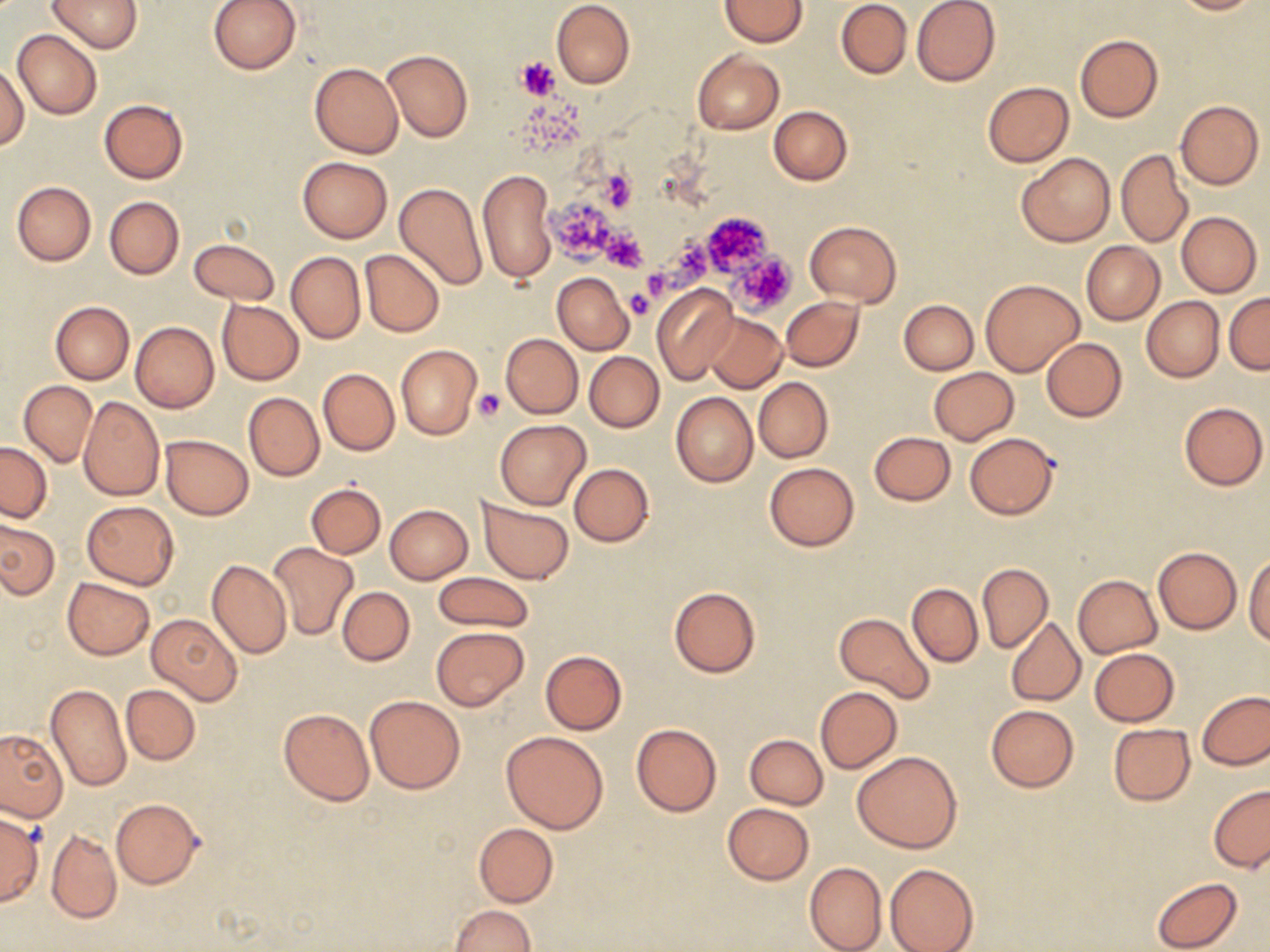
Summary:
  - Coordinate format: approximate bounding boxes as named x1/y1/x2/y2 corners in pixels
  - Platelet locations: (x1=514, y1=56, x2=560, y2=99), (x1=598, y1=166, x2=637, y2=213), (x1=549, y1=199, x2=618, y2=264), (x1=700, y1=212, x2=773, y2=276), (x1=601, y1=229, x2=647, y2=273), (x1=660, y1=234, x2=709, y2=286), (x1=732, y1=251, x2=797, y2=315), (x1=625, y1=290, x2=655, y2=319), (x1=474, y1=389, x2=504, y2=419)
  - Uninfected red blood cell locations: (x1=47, y1=0, x2=142, y2=53), (x1=209, y1=0, x2=300, y2=74), (x1=551, y1=0, x2=635, y2=88), (x1=720, y1=0, x2=808, y2=46), (x1=836, y1=0, x2=911, y2=79), (x1=912, y1=0, x2=1001, y2=86), (x1=1171, y1=0, x2=1259, y2=15), (x1=12, y1=29, x2=101, y2=120), (x1=1074, y1=34, x2=1163, y2=122), (x1=382, y1=49, x2=473, y2=141), (x1=692, y1=49, x2=784, y2=134), (x1=309, y1=62, x2=402, y2=158), (x1=1, y1=64, x2=28, y2=150), (x1=982, y1=81, x2=1073, y2=167), (x1=99, y1=99, x2=188, y2=184), (x1=1176, y1=100, x2=1264, y2=189), (x1=768, y1=105, x2=852, y2=185), (x1=1115, y1=149, x2=1193, y2=248), (x1=1016, y1=152, x2=1115, y2=247), (x1=296, y1=156, x2=393, y2=243), (x1=478, y1=170, x2=556, y2=283), (x1=12, y1=181, x2=96, y2=265), (x1=394, y1=181, x2=487, y2=290), (x1=104, y1=196, x2=184, y2=279), (x1=1176, y1=212, x2=1262, y2=296), (x1=805, y1=220, x2=901, y2=308), (x1=190, y1=239, x2=280, y2=306), (x1=1082, y1=241, x2=1164, y2=324), (x1=360, y1=248, x2=444, y2=337), (x1=286, y1=251, x2=365, y2=344), (x1=552, y1=272, x2=634, y2=355), (x1=980, y1=278, x2=1084, y2=377), (x1=651, y1=283, x2=739, y2=384), (x1=1225, y1=292, x2=1270, y2=373), (x1=782, y1=295, x2=864, y2=371), (x1=1141, y1=296, x2=1224, y2=382), (x1=216, y1=299, x2=304, y2=385), (x1=900, y1=300, x2=979, y2=374), (x1=50, y1=301, x2=134, y2=384), (x1=706, y1=313, x2=786, y2=391), (x1=131, y1=322, x2=219, y2=412), (x1=501, y1=333, x2=583, y2=419), (x1=1040, y1=337, x2=1126, y2=421), (x1=395, y1=344, x2=483, y2=441), (x1=584, y1=352, x2=664, y2=432), (x1=929, y1=368, x2=1019, y2=444), (x1=318, y1=369, x2=399, y2=455), (x1=753, y1=376, x2=833, y2=463), (x1=18, y1=380, x2=98, y2=466), (x1=243, y1=392, x2=323, y2=481), (x1=672, y1=393, x2=758, y2=487), (x1=78, y1=396, x2=164, y2=501), (x1=1179, y1=401, x2=1268, y2=490), (x1=496, y1=419, x2=589, y2=509), (x1=868, y1=431, x2=956, y2=505), (x1=964, y1=432, x2=1059, y2=519), (x1=160, y1=434, x2=253, y2=518), (x1=0, y1=441, x2=52, y2=522), (x1=764, y1=462, x2=860, y2=551), (x1=568, y1=463, x2=654, y2=547), (x1=307, y1=482, x2=385, y2=558), (x1=477, y1=499, x2=574, y2=583), (x1=81, y1=500, x2=179, y2=588), (x1=385, y1=504, x2=473, y2=584), (x1=0, y1=520, x2=59, y2=599), (x1=267, y1=543, x2=359, y2=641), (x1=1153, y1=546, x2=1242, y2=634), (x1=1245, y1=553, x2=1270, y2=644), (x1=207, y1=559, x2=291, y2=659), (x1=977, y1=561, x2=1053, y2=653), (x1=993, y1=568, x2=1072, y2=697), (x1=433, y1=571, x2=534, y2=631), (x1=1072, y1=574, x2=1161, y2=657), (x1=909, y1=575, x2=1049, y2=657), (x1=62, y1=577, x2=155, y2=660), (x1=907, y1=583, x2=982, y2=667), (x1=668, y1=586, x2=761, y2=677), (x1=337, y1=587, x2=415, y2=666), (x1=833, y1=612, x2=935, y2=704), (x1=148, y1=613, x2=243, y2=705), (x1=1006, y1=617, x2=1085, y2=706), (x1=432, y1=626, x2=528, y2=710), (x1=1088, y1=648, x2=1179, y2=726), (x1=540, y1=650, x2=626, y2=734), (x1=45, y1=683, x2=131, y2=790), (x1=121, y1=684, x2=200, y2=765), (x1=815, y1=687, x2=902, y2=773), (x1=1198, y1=691, x2=1270, y2=769), (x1=363, y1=695, x2=465, y2=793), (x1=986, y1=705, x2=1078, y2=791), (x1=279, y1=708, x2=374, y2=805), (x1=630, y1=722, x2=722, y2=817), (x1=1108, y1=723, x2=1194, y2=805), (x1=0, y1=729, x2=67, y2=822), (x1=501, y1=731, x2=609, y2=834), (x1=736, y1=733, x2=821, y2=880), (x1=744, y1=734, x2=829, y2=809), (x1=853, y1=750, x2=962, y2=853), (x1=1208, y1=784, x2=1270, y2=874), (x1=111, y1=798, x2=204, y2=889), (x1=722, y1=803, x2=814, y2=883), (x1=0, y1=812, x2=42, y2=905), (x1=472, y1=822, x2=558, y2=908), (x1=46, y1=829, x2=122, y2=924), (x1=804, y1=862, x2=887, y2=952), (x1=884, y1=863, x2=979, y2=952), (x1=1152, y1=876, x2=1242, y2=952), (x1=448, y1=904, x2=535, y2=952)
  - Slide-level diagnosis: negative for blood parasites
  - Field of view: one of a larger specimen
  - Stain: May-Grünwald-Giemsa
  - Magnification: 1000x
  - Preparation: thin blood film
  - Modality: optical microscopy
  - Image size: 1270×952 pixels